Locate every malaria parasite and every leukocyte.
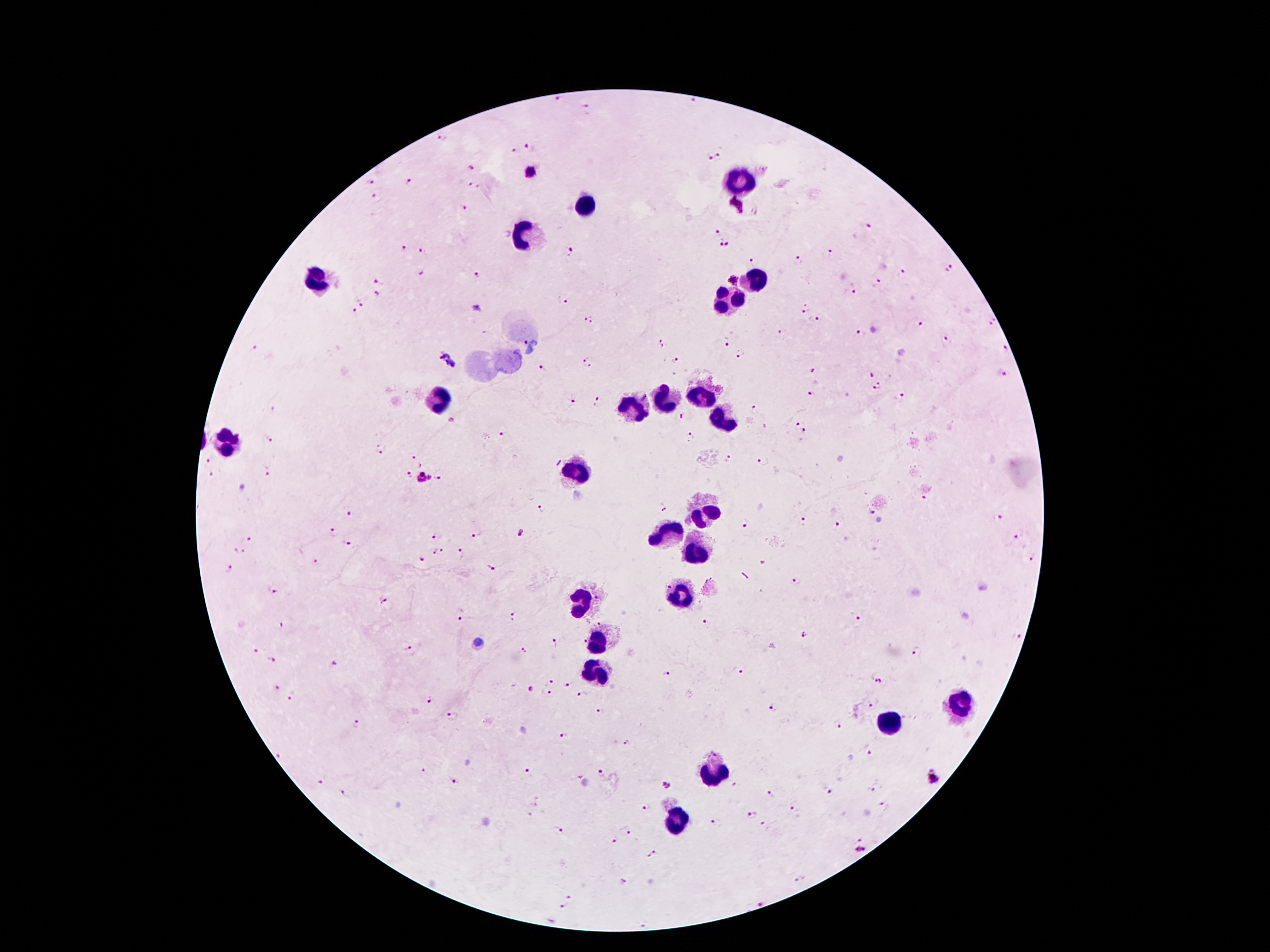

Approximate centers as (x, y) in pixels.
Malaria parasites: (560, 98), (693, 100), (589, 110), (440, 139), (529, 147), (511, 150), (714, 156), (471, 168), (532, 174), (371, 183), (410, 183), (474, 185), (734, 205), (466, 207), (755, 212), (868, 226), (718, 231), (725, 243), (404, 247), (571, 251), (422, 252), (830, 252), (798, 258), (752, 261), (950, 270), (902, 273), (421, 274), (477, 274), (379, 280), (733, 280), (878, 283), (379, 294), (852, 294), (561, 300), (361, 303), (804, 310), (355, 311), (818, 319), (587, 320), (993, 322), (919, 324), (780, 332), (860, 332), (948, 338), (525, 342), (727, 342), (661, 344), (256, 348), (1004, 351), (741, 355), (448, 361), (677, 361), (589, 362), (541, 366), (813, 372), (1003, 375), (871, 377), (878, 387), (811, 393), (900, 396), (599, 401), (571, 402), (756, 407), (682, 418), (796, 424), (804, 432), (504, 434), (691, 436), (270, 439), (383, 449), (419, 459), (729, 459), (763, 462), (207, 464), (267, 474), (408, 475), (440, 476), (211, 477), (422, 478), (924, 498), (664, 507), (542, 509), (873, 510), (349, 513), (1000, 517), (802, 520), (746, 525), (835, 525), (333, 532), (437, 535), (522, 535), (477, 536), (1016, 536), (249, 540), (346, 543), (241, 551), (439, 552), (460, 554), (1030, 558), (315, 561), (420, 561), (494, 566), (231, 568), (795, 582), (273, 590), (383, 602), (513, 615), (855, 617), (461, 618), (707, 624), (281, 626), (803, 636), (1016, 636), (556, 644), (407, 649), (523, 651), (915, 651), (254, 652), (273, 661), (333, 662), (740, 670), (667, 674), (879, 681), (552, 682), (568, 684), (276, 687), (530, 689), (548, 694), (582, 694), (291, 699), (428, 701), (872, 706), (773, 709), (599, 712), (452, 716), (356, 723), (837, 727), (565, 735), (627, 743), (869, 753), (281, 756), (425, 771), (529, 772), (602, 772), (934, 777), (456, 780), (323, 781), (666, 785), (871, 789), (828, 790), (345, 792), (770, 795), (884, 805), (648, 806), (793, 809), (752, 815), (717, 823), (762, 825), (626, 830), (559, 831), (615, 840), (860, 850), (654, 854), (799, 878), (626, 882), (569, 897), (564, 906).
Leukocytes: (740, 180), (582, 205), (525, 236), (754, 278), (317, 281), (731, 300), (699, 395), (437, 397), (660, 403), (633, 412), (717, 419), (226, 441), (578, 469), (703, 513), (664, 535), (695, 550), (680, 596), (579, 602), (600, 642), (596, 674), (955, 704), (889, 723), (715, 773), (677, 821).

Image is 1270×952 pixels. Thick blood smear. 100x magnification. Photographed through the microscope eyepiece with a smartphone camera. Giemsa-stained preparation. Patient malaria status: infected with Plasmodium falciparum. Single field of view.